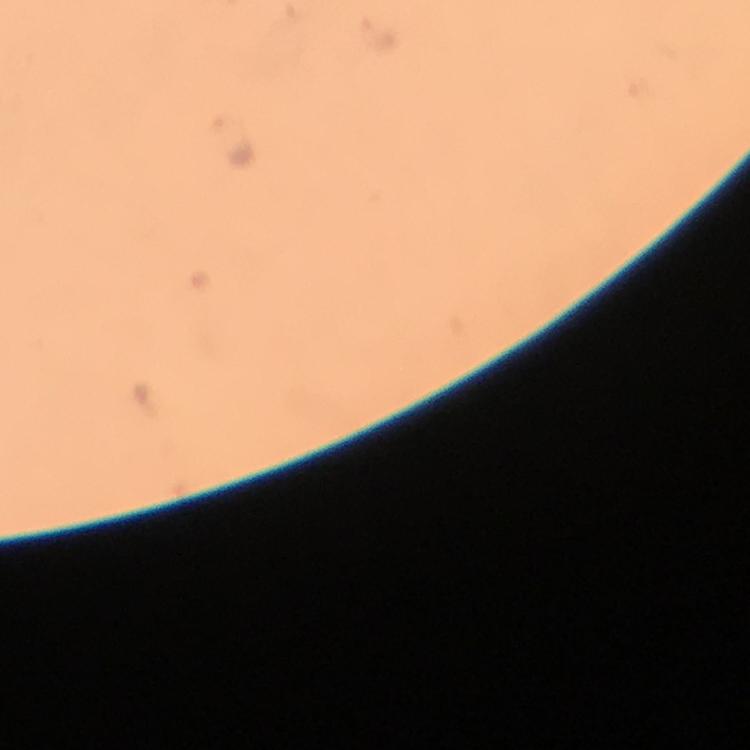

{
  "immersion_oil": "applied",
  "preparation": "thick smear",
  "cropped_from": "a single field of view",
  "magnification": "100x",
  "plasmodium_parasite_locations": "approximate object centers, in pixels from the top-left corner: (x=378, y=32), (x=230, y=142)",
  "capture": "smartphone photograph through a microscope",
  "context": "from a diagnostic examination for malaria",
  "image_size": "750×750 pixels",
  "stain": "Giemsa"
}